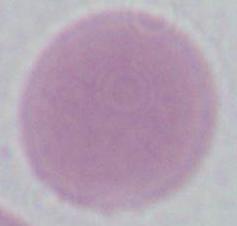
identification = red blood cell
modality = micrograph
magnification = 1000x